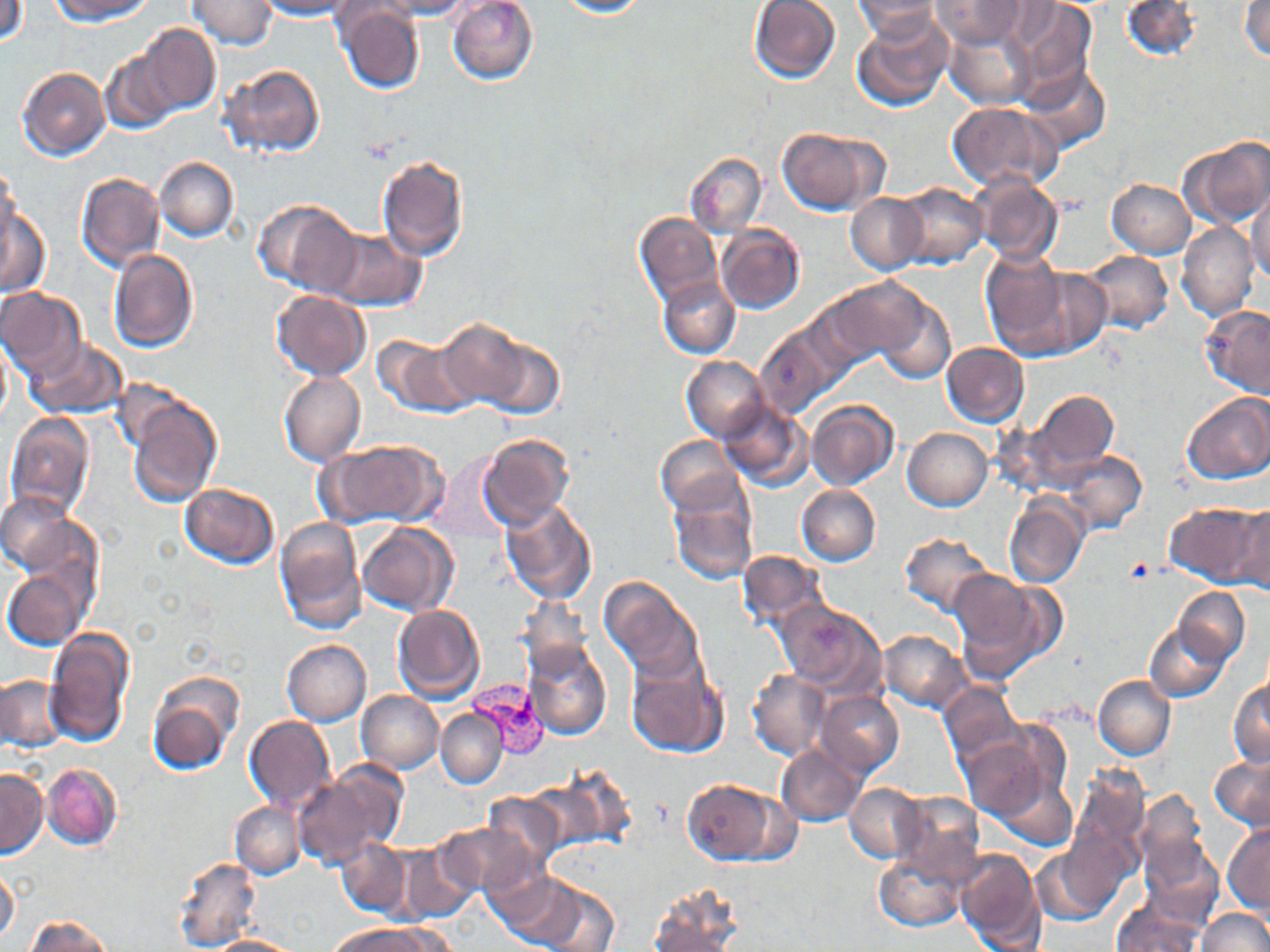

Summary:
  - Coordinate format: approximate bounding boxes as (x1, y1, x2, y2) in pixels
  - Uninfected red blood cell locations: (1, 0, 28, 46), (50, 0, 154, 22), (187, 0, 276, 50), (254, 0, 361, 19), (379, 0, 472, 18), (447, 0, 538, 85), (551, 0, 648, 18), (749, 0, 841, 83), (853, 0, 941, 41), (1004, 0, 1097, 101), (1120, 0, 1203, 62), (931, 1, 1027, 49), (1241, 2, 1269, 60), (336, 5, 425, 94), (852, 14, 953, 112), (945, 24, 1037, 111), (140, 25, 219, 115), (102, 49, 180, 133), (222, 64, 324, 156), (17, 67, 109, 160), (1018, 67, 1110, 155), (948, 101, 1059, 191), (778, 127, 888, 215), (1180, 136, 1270, 228), (684, 151, 766, 238), (375, 155, 468, 260), (155, 156, 238, 241), (1, 167, 19, 248), (75, 173, 164, 272), (971, 175, 1063, 265), (1107, 180, 1196, 257), (896, 183, 987, 267), (1247, 189, 1270, 285), (846, 194, 927, 273), (255, 199, 361, 294), (0, 207, 50, 297), (634, 212, 720, 304), (715, 223, 806, 314), (1178, 223, 1258, 321), (320, 227, 426, 312), (108, 248, 198, 352), (1079, 249, 1174, 334), (980, 252, 1082, 358), (1015, 267, 1112, 357), (657, 277, 740, 359), (823, 277, 935, 366), (1, 288, 86, 379), (272, 290, 369, 381), (867, 292, 956, 386), (1200, 306, 1270, 400), (433, 319, 531, 411), (755, 324, 843, 417), (370, 335, 467, 416), (0, 337, 12, 428), (23, 338, 127, 419), (476, 338, 565, 418), (940, 342, 1030, 427), (682, 356, 770, 442), (278, 371, 366, 467), (1025, 389, 1119, 484), (1181, 393, 1270, 484), (126, 398, 221, 507), (806, 400, 898, 491), (717, 402, 812, 491), (4, 414, 94, 519), (902, 428, 992, 511), (476, 432, 575, 529), (655, 436, 746, 517), (319, 438, 446, 526), (1060, 452, 1146, 534), (181, 484, 280, 568), (797, 484, 880, 566), (1, 493, 82, 575), (669, 493, 757, 585), (500, 498, 597, 603), (1004, 498, 1086, 588), (1165, 502, 1267, 586), (1231, 503, 1270, 594), (274, 519, 367, 634), (356, 522, 457, 615), (899, 532, 994, 615), (737, 550, 827, 630), (4, 569, 89, 649), (954, 569, 1058, 679), (599, 577, 705, 683), (1174, 588, 1249, 663), (518, 596, 594, 677), (775, 601, 885, 695), (392, 605, 485, 702), (1144, 623, 1231, 703), (43, 627, 137, 747), (877, 629, 972, 713), (522, 639, 612, 740), (282, 640, 371, 725), (624, 656, 729, 758), (747, 669, 830, 760), (145, 674, 243, 773), (0, 675, 65, 753), (1093, 675, 1175, 761), (1228, 680, 1270, 766), (940, 683, 1021, 765), (356, 691, 444, 774), (817, 691, 904, 777), (436, 709, 508, 788), (245, 717, 336, 813), (958, 733, 1057, 822), (777, 745, 866, 827), (1209, 756, 1270, 831), (42, 764, 122, 850), (550, 764, 638, 848), (1066, 766, 1149, 869), (989, 767, 1077, 850), (0, 769, 47, 857), (292, 772, 399, 871), (681, 780, 780, 865), (846, 784, 924, 862), (1132, 789, 1211, 882), (481, 791, 566, 868), (892, 792, 984, 881), (230, 801, 304, 879), (433, 821, 539, 899), (1223, 824, 1269, 913), (1136, 835, 1223, 928), (336, 838, 409, 917), (1032, 841, 1127, 925), (392, 846, 475, 923), (955, 848, 1044, 951), (874, 851, 967, 932), (171, 856, 260, 952), (0, 868, 19, 944), (488, 869, 583, 946), (533, 882, 620, 952), (647, 887, 743, 949), (1111, 898, 1204, 952), (1198, 908, 1268, 952), (25, 916, 113, 952), (330, 922, 429, 952), (208, 935, 299, 952)
  - Plasmodium vivax-infected red blood cell locations: (464, 681, 550, 757)
  - Platelet locations: (1122, 558, 1156, 586)
  - Slide-level diagnosis: Plasmodium vivax
  - Image size: 1270×952 pixels
  - Magnification: 1000x
  - Preparation: thin blood smear
  - Stain: May-Grünwald-Giemsa
  - Field of view: one of a larger specimen
  - Modality: optical microscopy